Draw a bounding box around every parasitised red blood cell, every trophozoite, every gametocyte, every leukocyte, and every artifact (platelet-like body, stain precipitate, or debris).
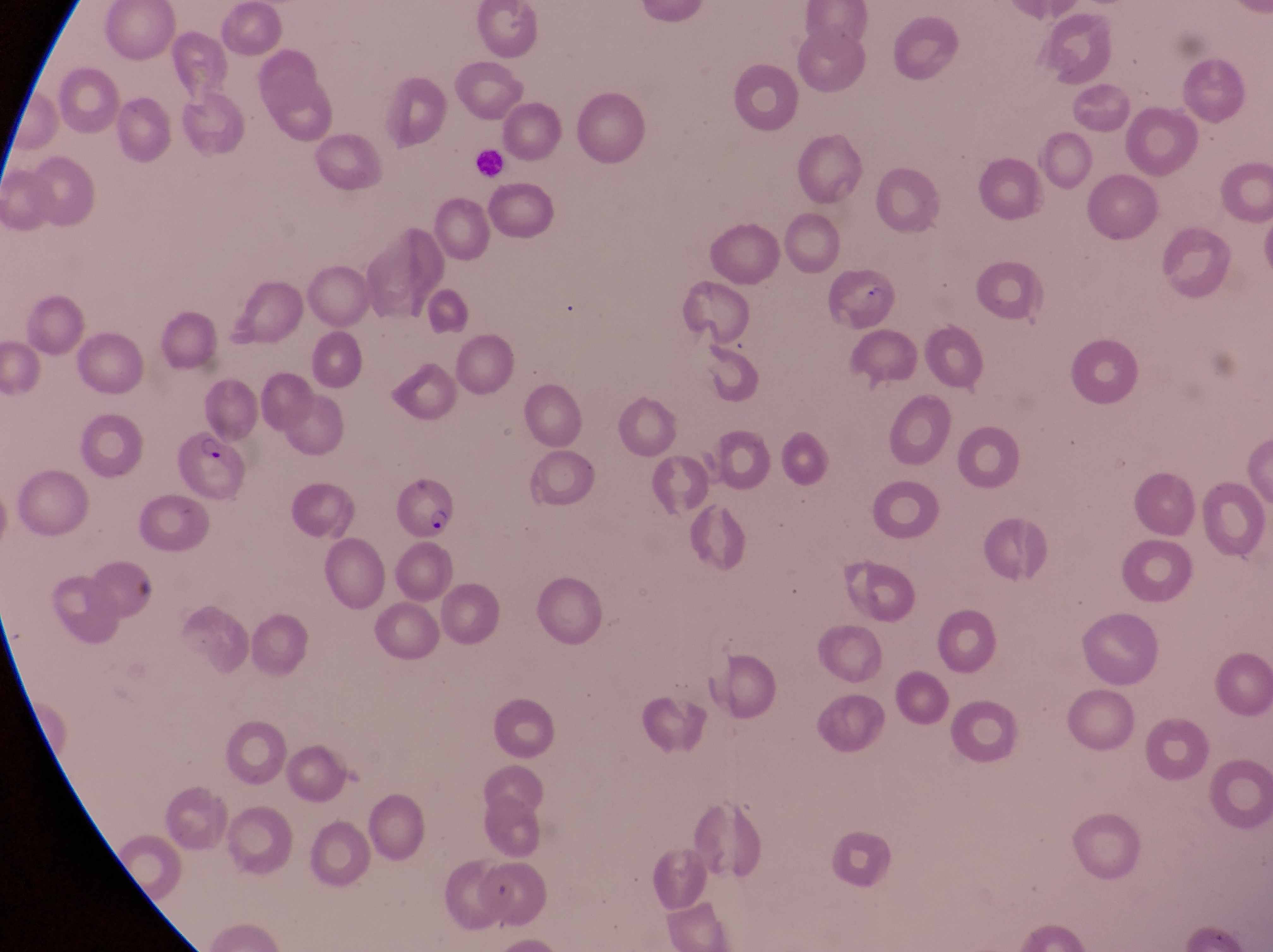
Approximate bounding boxes as (left, top, right, bottom) in pixels.
Parasitised red blood cells: (829, 268, 895, 334), (178, 430, 256, 504), (395, 475, 453, 542).
Leukocytes: (473, 147, 504, 178).

Magnification of 1000x. Thin blood film. One field of view. Captured by a smartphone held over the eyepiece of an Olympus CX-23 microscope. Image is 1273×952 pixels. Sample from Uganda.